Assess this cell for malaria.
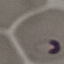

It is parasitized.

image type = cell patch, automatically extracted from a larger field of view and resized to 64 × 64 pixels
stain = Giemsa
capture = smartphone camera at the microscope eyepiece
preparation = thin blood smear